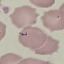
Result: no malaria parasites seen. Photographed with a smartphone camera at the microscope eyepiece. Cell patch, automatically extracted from a larger field of view and resized to 64 × 64 pixels. Thin blood smear. Giemsa stain.